Point out each Plasmodium parasite.
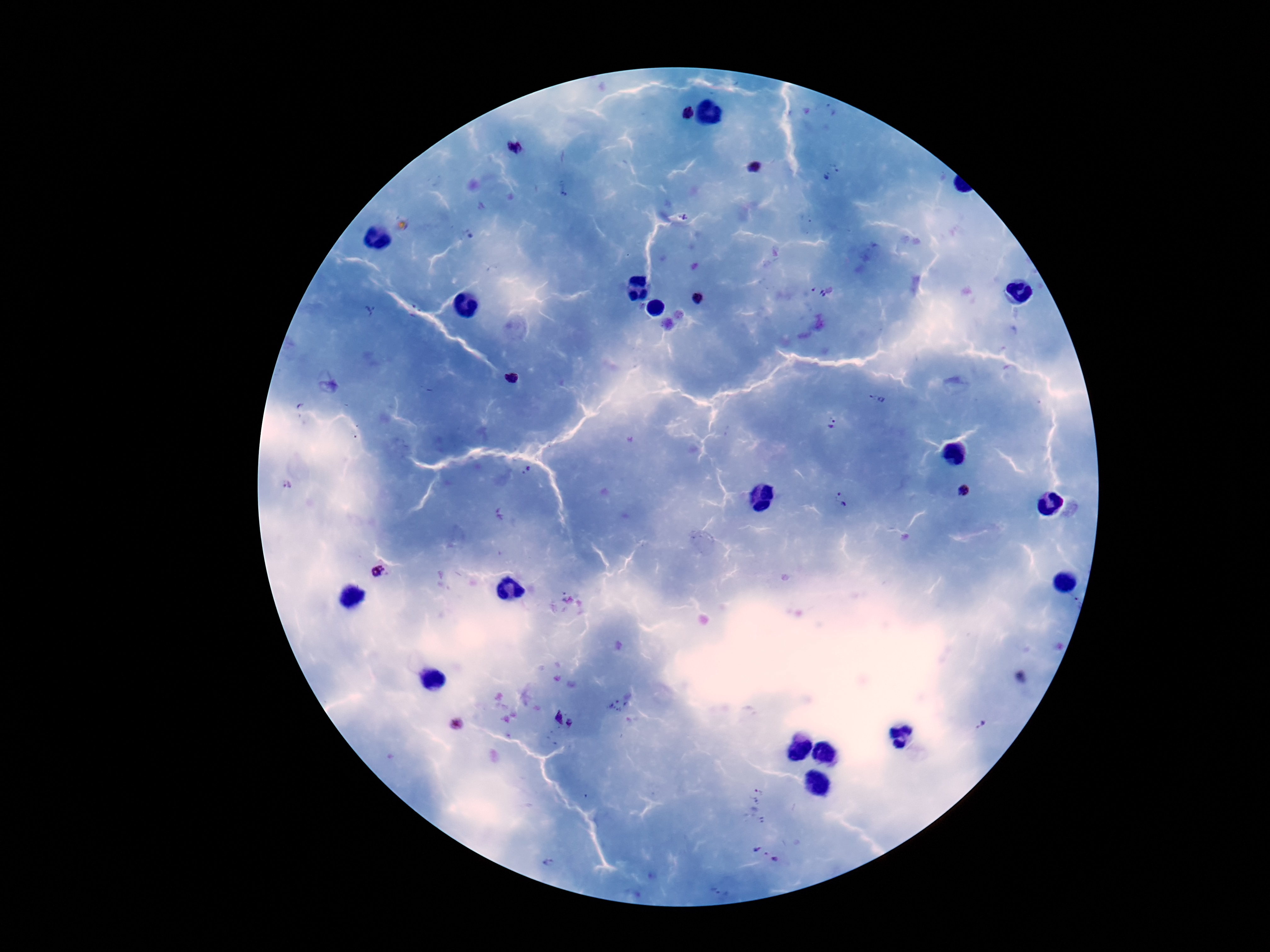

Approximate centers as (x, y) in pixels.
Plasmodium parasites: (689, 111), (514, 147), (754, 168), (831, 172), (822, 288), (697, 300), (512, 377), (878, 399), (832, 424), (526, 470), (287, 484), (964, 490), (842, 500), (377, 571), (555, 716), (571, 724), (981, 724), (457, 725), (758, 791), (757, 848), (766, 854), (776, 862), (547, 863).

Summary:
  - Preparation: thick blood film
  - Patient malaria status: positive
  - Stain: Giemsa
  - Image size: 1270×952 pixels
  - Magnification: 100x
  - Capture: smartphone camera through the microscope eyepiece
  - Field of view: single